Report the malaria status of this cell.
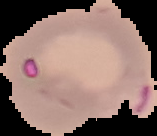

Parasitized.

Image is 157×136 pixels. From a thin blood smear. Cell region segmented out of the field of view; the surrounding area is masked to black.